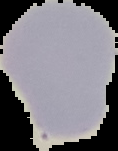
image type = segmented cell region on a black background
image size = 118×151 pixels
malaria status = uninfected
preparation = thin blood film